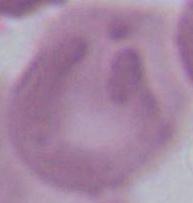
Summary:
  - Identification: red blood cell
  - Magnification: 1000x
  - Modality: photomicrograph